Point out each malaria parasite.
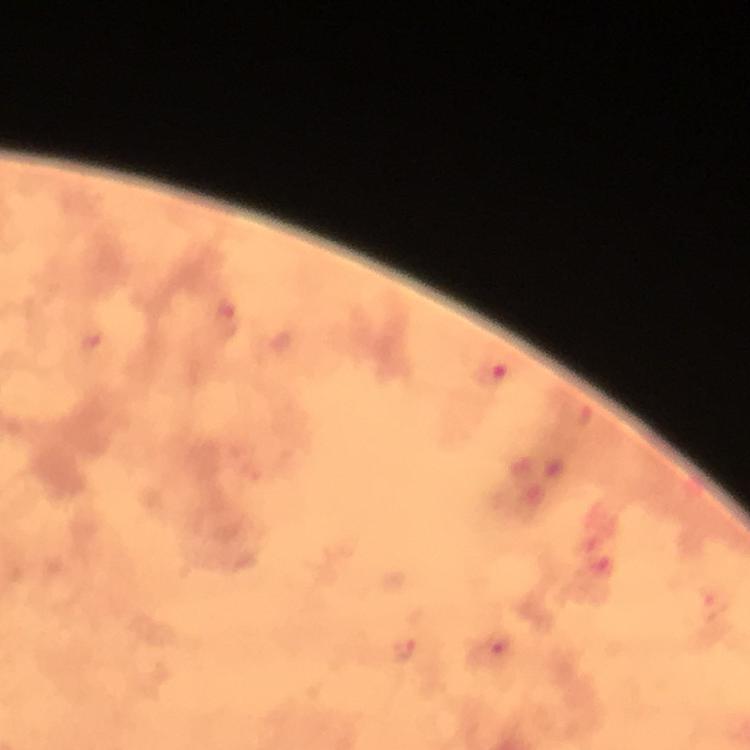
Approximate centers as (x, y) in pixels.
Malaria parasites: (224, 313), (489, 375), (492, 648), (402, 650).

stain: Giemsa
cropped_from: a single field of view
immersion_oil: used
image_size: 750×750 pixels
magnification: 100x
context: from a diagnostic examination for malaria
capture: smartphone camera through the microscope
preparation: thick blood film